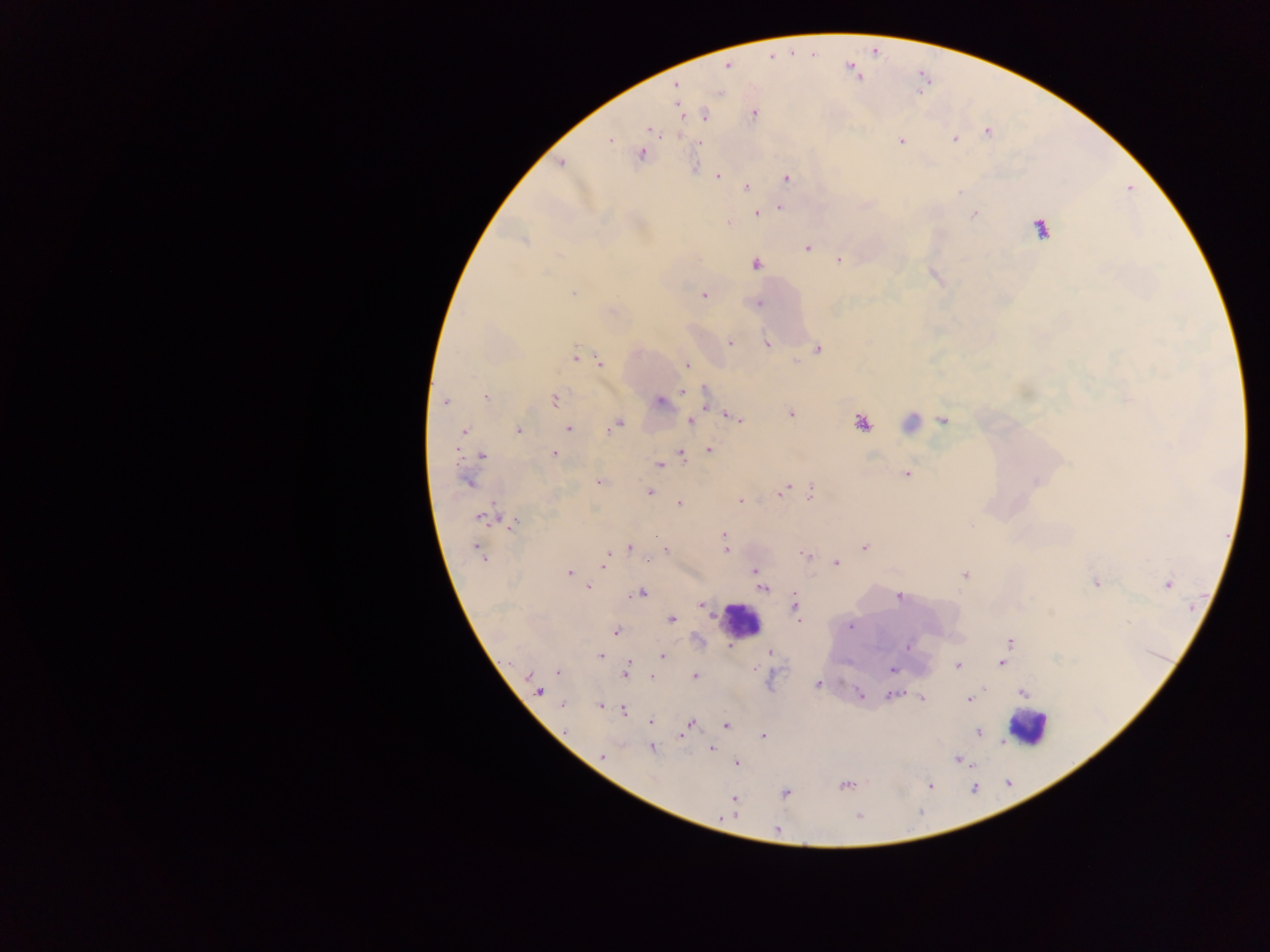

Approximate centers as x y in pixels.
Summary:
  - Malaria parasite locations: 846 67; 856 75; 861 77; 678 85; 678 107; 753 114; 646 129; 678 136; 610 139; 900 139; 955 140; 641 153; 560 163; 695 163; 718 176; 787 179; 747 187; 780 207; 755 213; 728 221; 1039 228; 522 240; 806 248; 839 260; 755 263; 704 296; 757 304; 729 342; 767 344; 818 349; 575 356; 600 362; 687 364; 1020 390; 684 392; 485 397; 554 400; 446 401; 657 401; 705 406; 789 414; 727 415; 944 420; 690 421; 621 422; 862 422; 568 429; 610 429; 464 431; 519 431; 605 432; 709 449; 682 453; 456 454; 482 454; 553 454; 658 465; 908 472; 598 481; 468 482; 649 491; 810 492; 781 493; 740 500; 678 503; 493 506; 480 519; 515 522; 723 536; 726 545; 477 546; 865 547; 632 548; 725 549; 665 550; 607 553; 804 555; 836 563; 603 565; 753 570; 963 574; 569 575; 1097 583; 1168 584; 589 586; 763 588; 644 592; 898 598; 795 601; 672 619; 798 620; 849 626; 615 631; 1010 642; 908 645; 730 646; 770 653; 600 655; 662 657; 1004 664; 628 665; 957 666; 756 669; 892 669; 526 675; 624 675; 694 677; 818 685; 541 692; 1022 693; 859 694; 895 694; 922 699; 970 701; 561 705; 599 706; 623 710; 652 722; 726 726; 722 728; 685 732; 979 733; 681 736; 764 736; 652 748; 711 748; 603 757; 957 759; 735 764; 844 788; 785 793; 734 798; 732 813; 860 816
  - Leukocyte locations: 738 618; 1027 730
  - Image size: 1270×952 pixels
  - Field of view: single
  - Country: Ghana
  - Preparation: thick blood film
  - Capture: mobile-phone photograph through a microscope